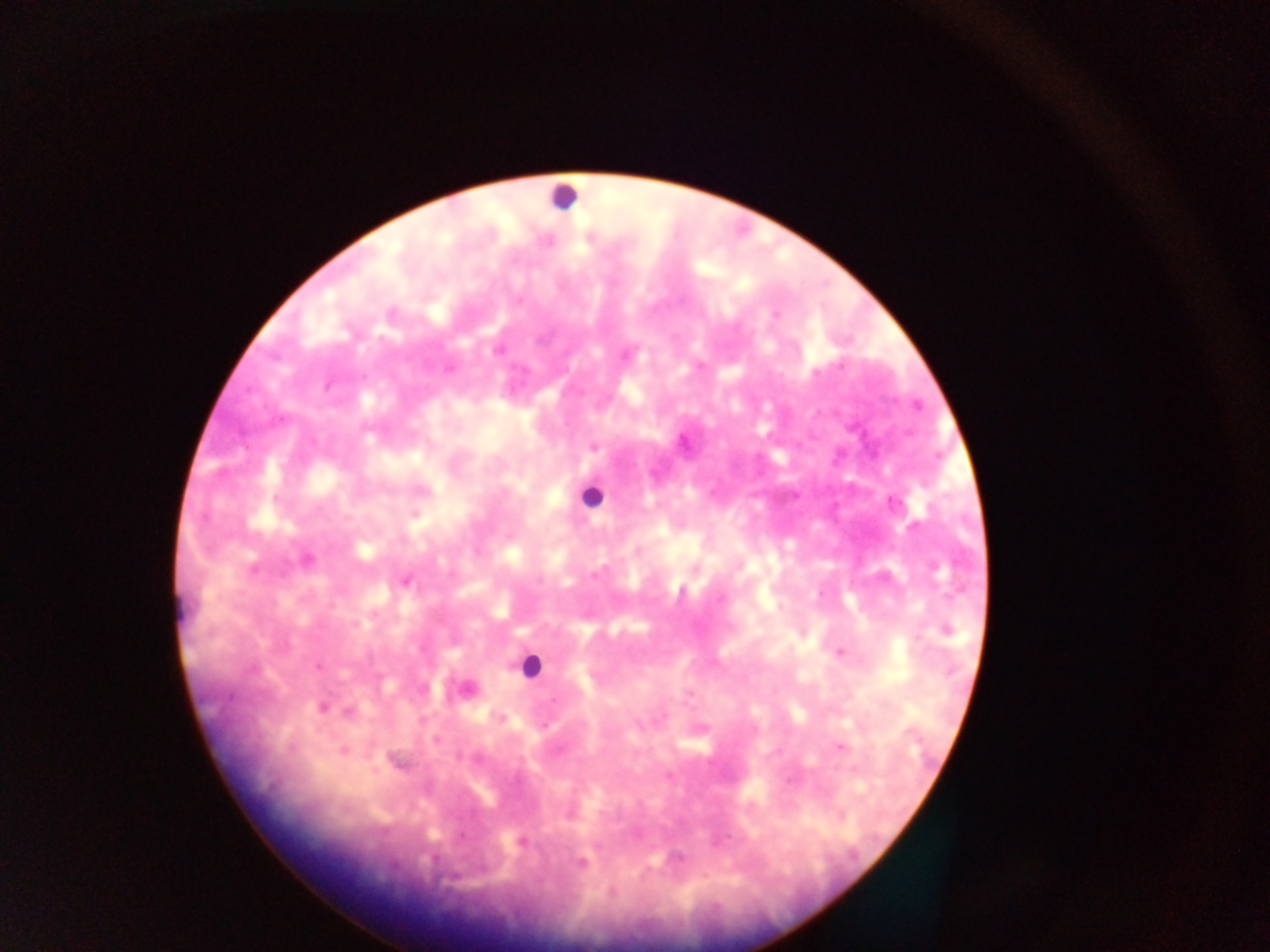

Approximate centers as (x, y) in pixels.
Summary:
  - Leukocyte locations: (562, 195), (590, 495), (530, 665)
  - Malaria parasite locations: (497, 349), (625, 354), (448, 368), (592, 446), (892, 503), (638, 550), (305, 560), (405, 580), (946, 630), (839, 652), (466, 688), (687, 693), (321, 707), (349, 710), (840, 747), (344, 751), (569, 811), (521, 842), (580, 862), (611, 892)
  - Field of view: single
  - Capture: mobile-phone photograph through a microscope
  - Image size: 1270×952 pixels
  - Country: Ghana
  - Preparation: thick blood film